Mark where platelets are.
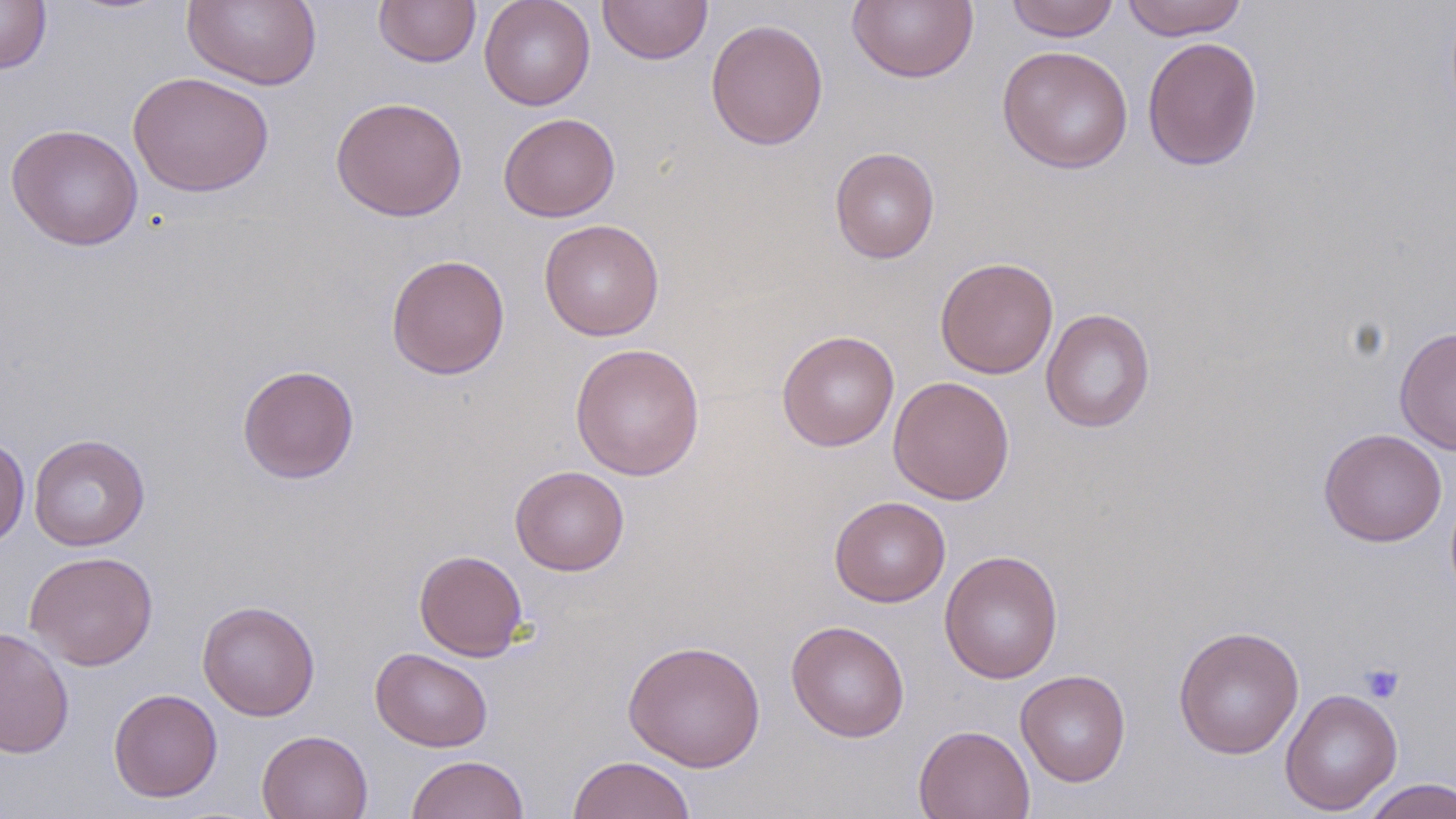

Approximate bounding boxes as (x1, y1, x2, y2) in pixels.
Platelets: (1359, 662, 1405, 704).

Summary:
  - Uninfected red blood cell locations: (0, 0, 52, 75), (182, 0, 321, 90), (373, 0, 481, 67), (479, 0, 596, 111), (597, 0, 712, 65), (847, 0, 978, 84), (1005, 0, 1120, 42), (1121, 0, 1249, 40), (705, 19, 828, 150), (1142, 36, 1263, 171), (996, 45, 1134, 173), (128, 71, 275, 197), (330, 96, 468, 221), (498, 112, 621, 222), (6, 123, 144, 250), (829, 147, 940, 264), (539, 219, 665, 341), (386, 254, 510, 380), (934, 257, 1059, 379), (1041, 308, 1156, 433), (1394, 326, 1456, 455), (776, 330, 899, 451), (569, 342, 705, 481), (237, 364, 360, 484), (888, 375, 1015, 505), (1318, 428, 1447, 547), (28, 433, 150, 551), (0, 436, 30, 548), (510, 465, 629, 576), (829, 495, 951, 607), (414, 549, 528, 661), (939, 549, 1064, 684), (24, 551, 159, 670), (197, 599, 321, 721), (786, 620, 910, 742), (1173, 625, 1305, 760), (0, 626, 74, 759), (623, 639, 766, 772), (370, 647, 493, 752), (1015, 669, 1131, 787), (1279, 687, 1403, 815), (108, 688, 223, 802), (913, 724, 1035, 819), (256, 729, 373, 819), (406, 754, 529, 819), (568, 755, 697, 819), (1359, 778, 1456, 819)
  - Slide-level diagnosis: negative for blood parasites
  - Stain: May-Grünwald-Giemsa
  - Image size: 1456×819 pixels
  - Magnification: 1000x
  - Preparation: thin blood film
  - Field of view: one of a larger specimen
  - Modality: optical microscopy